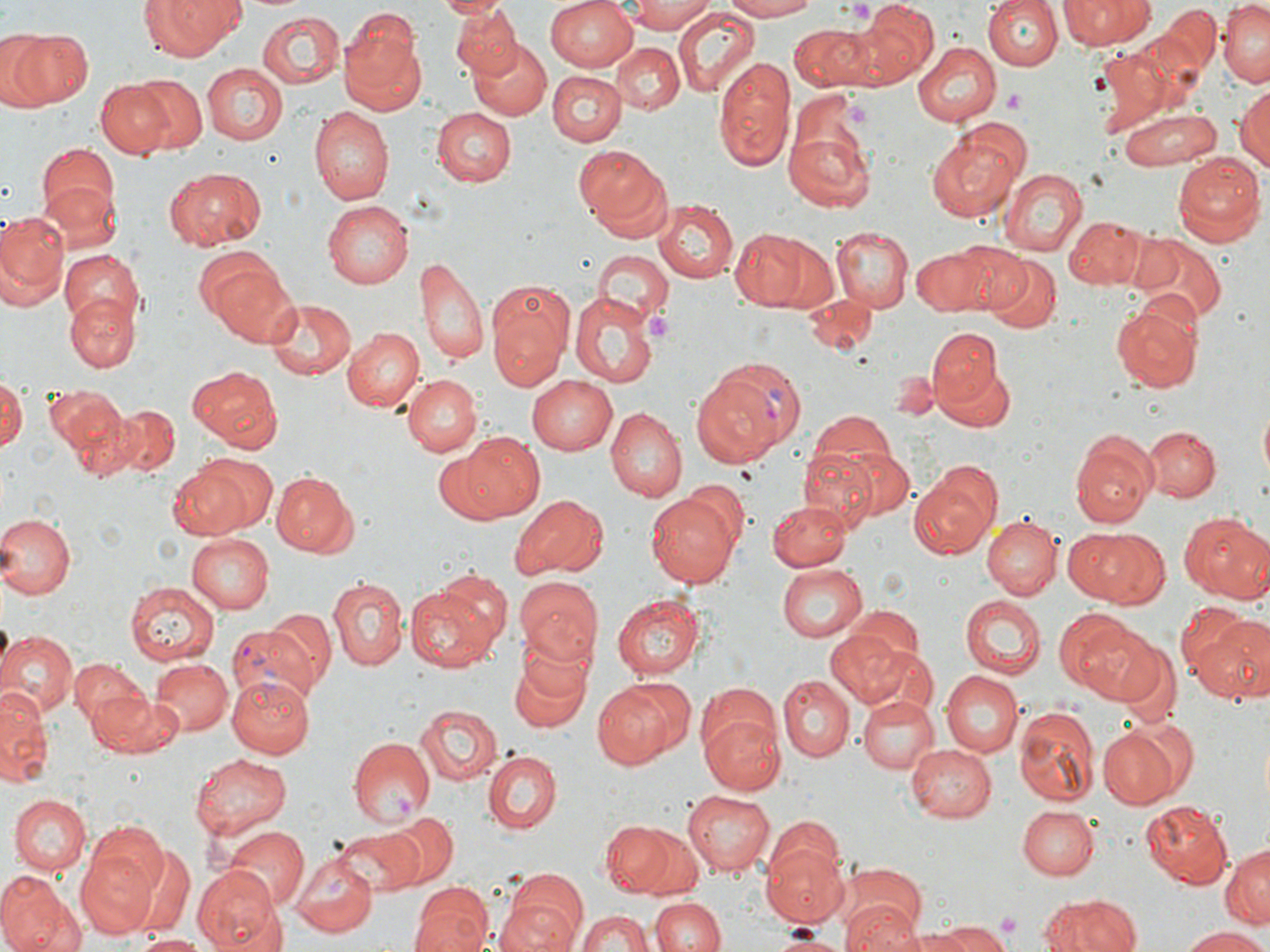
slide-level diagnosis = Plasmodium vivax
preparation = thin blood smear
platelet locations = approximate bounding boxes as [x1, y1, x2, y2] in pixels: [851, 1, 874, 23], [1004, 90, 1026, 112], [843, 100, 876, 128], [645, 313, 674, 341], [992, 911, 1023, 938]
stain = May-Grünwald-Giemsa
image size = 1270×952 pixels
field of view = one of a larger specimen
modality = light microscopy
magnification = 1000x
uninfected red blood cell locations = approximate bounding boxes as [x1, y1, x2, y2] in pixels: [139, 0, 248, 64], [435, 0, 508, 19], [547, 0, 640, 71], [718, 0, 825, 21], [984, 0, 1062, 72], [1060, 0, 1153, 47], [1220, 0, 1269, 85], [623, 1, 717, 33], [449, 3, 521, 80], [858, 3, 940, 84], [1161, 6, 1222, 78], [672, 8, 761, 98], [255, 12, 344, 89], [338, 21, 427, 116], [790, 24, 870, 90], [3, 27, 93, 111], [470, 41, 552, 121], [612, 41, 683, 113], [913, 41, 1000, 124], [713, 56, 796, 171], [201, 63, 289, 145], [548, 70, 623, 145], [125, 73, 208, 155], [94, 80, 176, 158], [1232, 82, 1270, 172], [308, 106, 393, 204], [432, 107, 516, 185], [1118, 107, 1223, 168], [784, 125, 875, 215], [926, 133, 1023, 221], [573, 144, 673, 240], [34, 145, 116, 228], [1171, 154, 1264, 245], [164, 167, 266, 251], [998, 168, 1087, 255], [39, 180, 121, 252], [653, 199, 739, 282], [323, 200, 414, 288], [0, 210, 69, 312], [1064, 216, 1144, 290], [729, 227, 834, 313], [833, 227, 912, 312], [829, 234, 992, 315], [1133, 236, 1227, 327], [950, 243, 1030, 316], [912, 244, 998, 317], [194, 245, 296, 345], [590, 249, 671, 330], [58, 251, 145, 336], [418, 254, 489, 371], [982, 254, 1062, 332], [486, 278, 575, 391], [65, 291, 137, 371], [570, 293, 657, 390], [802, 296, 878, 355], [262, 297, 355, 380], [1111, 304, 1200, 392], [344, 327, 426, 413], [927, 328, 1007, 417], [186, 364, 282, 446], [890, 365, 939, 420], [0, 372, 25, 456], [402, 373, 482, 456], [528, 374, 618, 455], [42, 385, 127, 460], [1258, 402, 1270, 484], [110, 403, 179, 478], [605, 406, 686, 503], [806, 410, 901, 490], [1142, 425, 1220, 501], [459, 431, 545, 519], [1071, 431, 1158, 527], [825, 447, 915, 526], [800, 448, 877, 528], [430, 450, 517, 524], [167, 459, 257, 537], [911, 465, 1002, 557], [269, 470, 357, 556], [685, 479, 749, 550], [645, 494, 740, 586], [513, 495, 608, 580], [768, 498, 852, 571], [1180, 512, 1270, 603], [0, 513, 74, 597], [983, 516, 1062, 600], [1068, 527, 1163, 607], [184, 533, 274, 615], [774, 562, 867, 643], [514, 575, 602, 668], [330, 578, 406, 670], [126, 580, 221, 663], [406, 585, 498, 674], [612, 594, 704, 679], [960, 595, 1046, 678], [842, 604, 923, 674], [1053, 606, 1152, 701], [267, 608, 336, 690], [1190, 616, 1270, 704], [0, 630, 77, 719], [824, 631, 910, 709], [507, 638, 594, 735], [1109, 639, 1181, 730], [852, 640, 939, 718], [150, 658, 232, 737], [71, 660, 150, 728], [942, 672, 1024, 758], [228, 674, 318, 758], [778, 677, 853, 762], [595, 678, 688, 768], [0, 689, 49, 785], [90, 689, 179, 756], [857, 695, 940, 774], [415, 704, 502, 784], [1014, 708, 1097, 809], [699, 710, 786, 797], [1098, 722, 1185, 808], [348, 736, 433, 827], [907, 743, 1000, 822], [484, 751, 559, 834], [192, 753, 293, 838], [683, 790, 777, 876], [9, 794, 90, 874], [1139, 801, 1233, 891], [1017, 806, 1096, 880], [383, 810, 458, 888], [763, 815, 846, 896], [600, 817, 700, 899], [223, 827, 307, 911], [335, 828, 424, 894], [75, 839, 166, 938], [760, 843, 849, 927], [1221, 843, 1270, 930], [124, 846, 195, 936], [291, 852, 378, 936], [193, 867, 283, 952], [0, 872, 74, 952], [498, 872, 589, 951], [837, 878, 928, 952], [410, 882, 492, 952], [1039, 890, 1144, 952], [650, 896, 724, 952], [575, 908, 655, 952], [933, 923, 1012, 952], [1182, 928, 1270, 952], [766, 930, 851, 950], [885, 931, 977, 952], [132, 934, 208, 950]
Plasmodium vivax-infected red blood cell locations = approximate bounding boxes as [x1, y1, x2, y2] in pixels: [691, 365, 794, 465], [229, 617, 328, 707]